Describe the morphology of the erythrocytes.
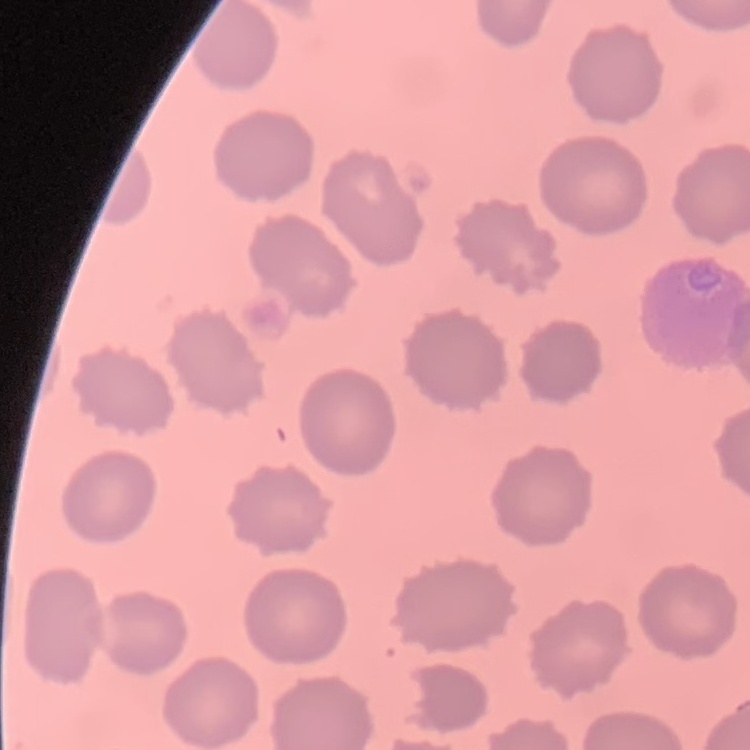
No rouleaux formation.

Summary:
  - Image type: square crop of a larger photomicrograph
  - Preparation: thin blood film
  - Stain: Field's or Giemsa